Identify the parasite.
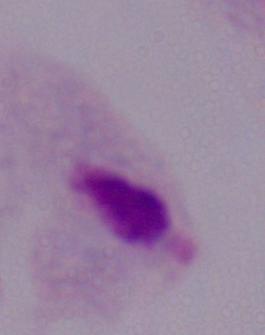

A trichomonad.

Summary:
  - Modality: micrograph
  - Magnification: 1000x